Evaluate for malaria.
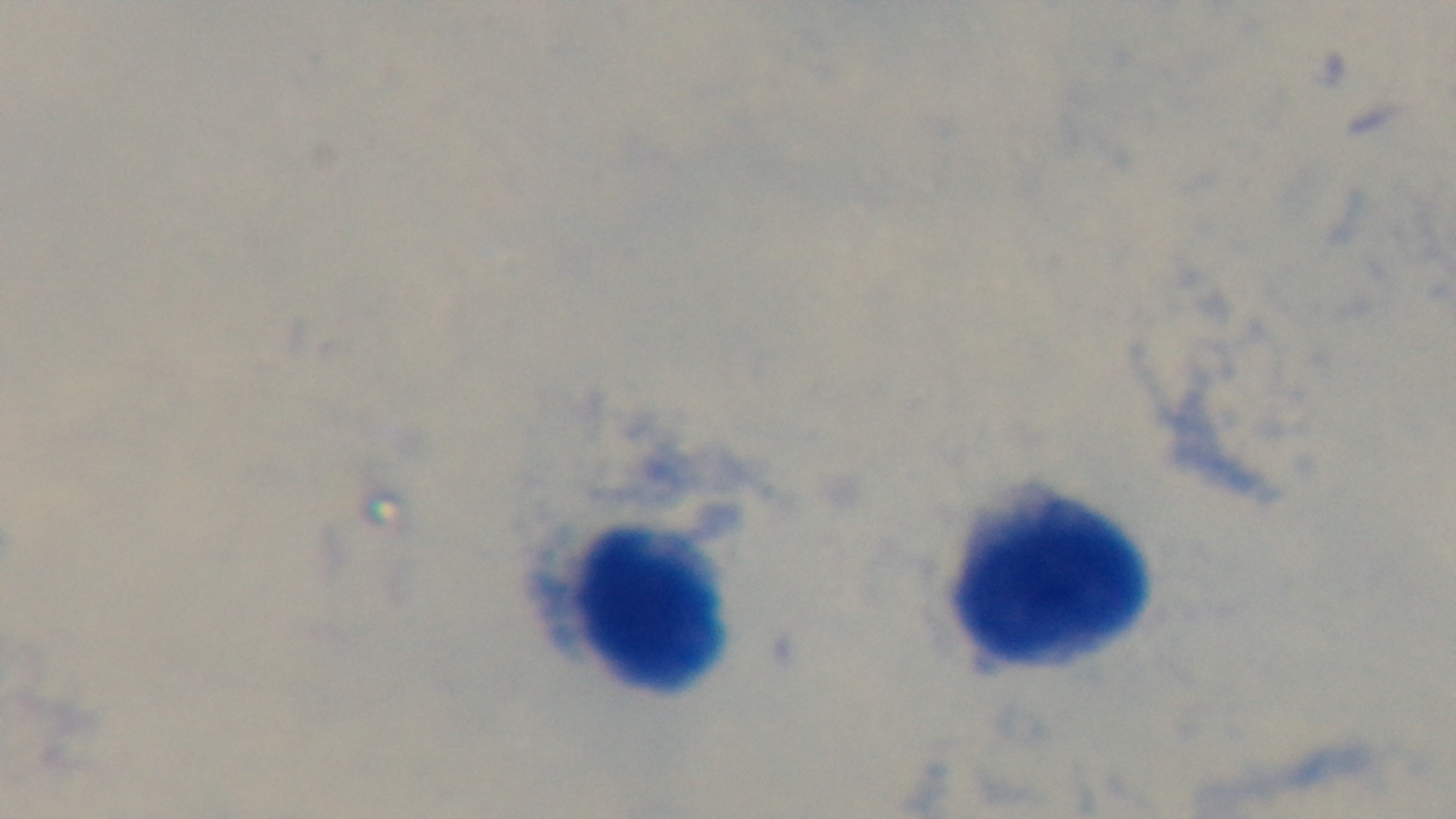
Negative.

capture = mounted 4K digital camera
objective = 100x oil immersion
stain = Giemsa
preparation = thick smear
field of view = single
modality = light microscopy